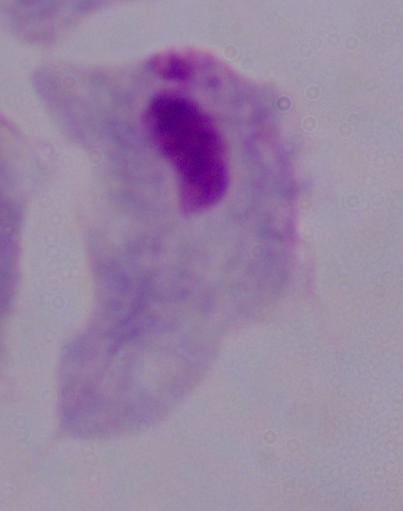

magnification = 1000x
identification = trichomonad
modality = micrograph